Outline each Plasmodium vivax-infected red blood cell.
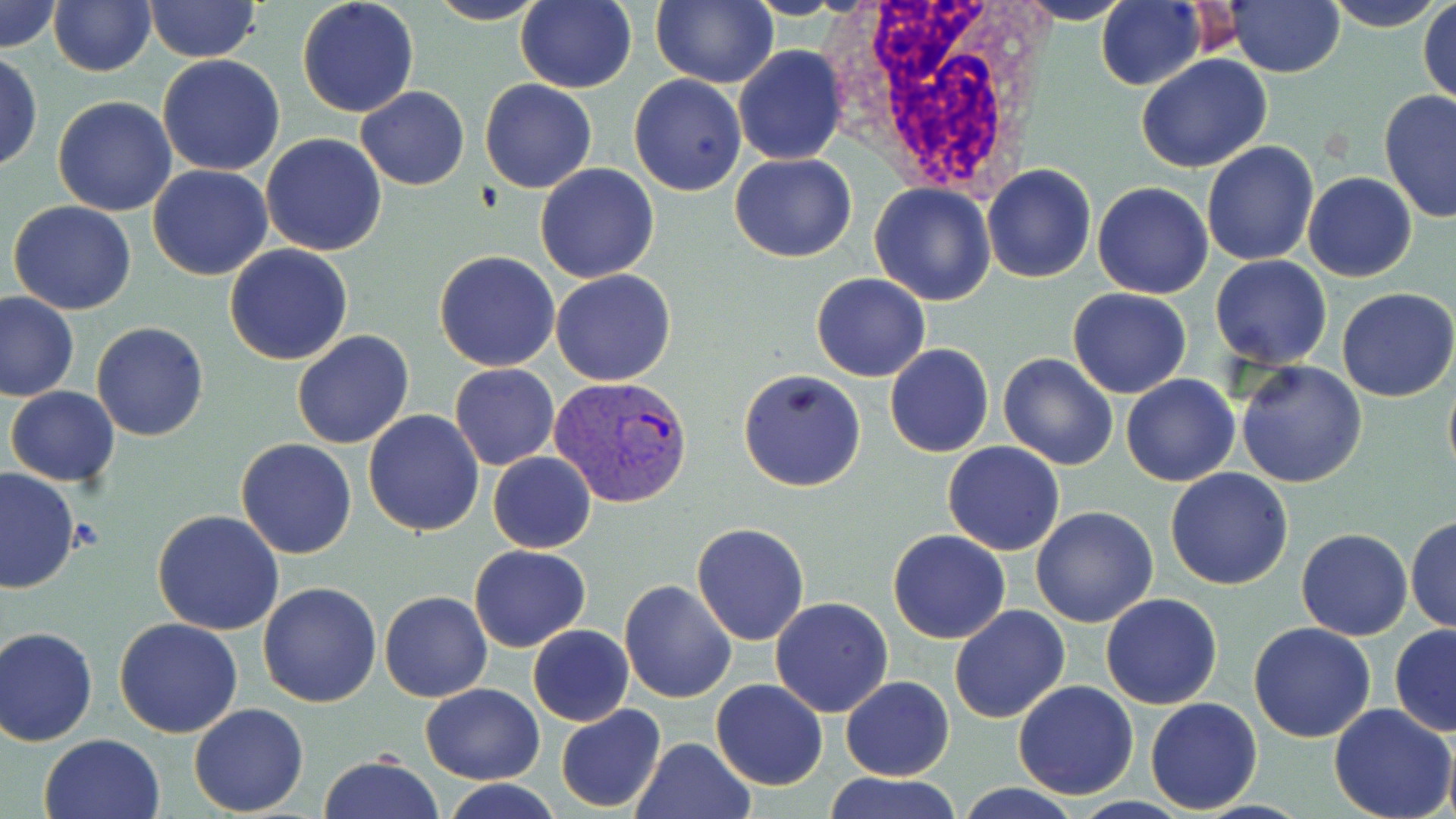

Approximate bounding boxes as [x1, y1, x2, y2] in pixels.
Plasmodium vivax-infected red blood cells: [549, 375, 695, 509].

White blood cell locations: [832, 0, 1054, 196]. Platelet locations: [72, 517, 104, 551]. Uninfected red blood cell locations: [1, 0, 63, 54], [146, 0, 260, 62], [297, 0, 419, 118], [651, 0, 779, 88], [1320, 0, 1445, 31], [48, 1, 156, 76], [424, 1, 550, 26], [515, 1, 636, 93], [1014, 1, 1135, 24], [1096, 1, 1203, 89], [1225, 1, 1344, 77], [1418, 1, 1455, 111], [734, 46, 849, 165], [1, 48, 42, 175], [156, 54, 286, 176], [1136, 54, 1274, 173], [629, 73, 746, 195], [479, 78, 597, 194], [355, 86, 469, 189], [1379, 91, 1456, 223], [52, 96, 179, 217], [260, 133, 387, 256], [1201, 141, 1321, 265], [729, 152, 857, 262], [533, 163, 659, 283], [148, 164, 272, 281], [982, 164, 1097, 284], [1302, 171, 1417, 282], [1092, 181, 1215, 299], [868, 183, 997, 306], [7, 201, 137, 316], [223, 244, 354, 366], [434, 250, 562, 371], [1209, 256, 1332, 370], [551, 268, 675, 386], [810, 273, 930, 382], [1067, 287, 1193, 399], [1336, 287, 1455, 401], [1, 292, 78, 402], [91, 321, 209, 440], [292, 330, 415, 449], [883, 343, 994, 458], [998, 351, 1120, 470], [1236, 359, 1368, 487], [450, 363, 560, 469], [1443, 368, 1456, 488], [738, 369, 866, 492], [1121, 374, 1240, 487], [6, 385, 120, 489], [363, 408, 486, 536], [237, 439, 357, 558], [942, 440, 1065, 557], [488, 451, 596, 553], [1, 468, 78, 594], [1165, 468, 1296, 589], [1030, 506, 1159, 628], [152, 510, 285, 635], [1404, 516, 1455, 634], [691, 522, 811, 645], [1296, 527, 1413, 641], [887, 530, 1012, 644], [468, 545, 590, 651], [619, 580, 738, 702], [258, 581, 382, 706], [380, 590, 493, 704], [1100, 593, 1223, 709], [769, 597, 893, 718], [949, 604, 1070, 724], [112, 619, 243, 738], [1248, 622, 1377, 743], [1389, 623, 1456, 737], [1, 624, 100, 747], [527, 625, 634, 726], [840, 676, 954, 781], [711, 679, 828, 790], [1012, 679, 1139, 799], [420, 683, 546, 782], [1145, 696, 1262, 815], [1329, 703, 1455, 819], [189, 704, 309, 816], [555, 705, 668, 814], [1441, 730, 1456, 819], [39, 734, 165, 819], [630, 736, 757, 819], [318, 753, 442, 819], [822, 771, 963, 819], [444, 780, 564, 818]. Slide-level diagnosis: Plasmodium vivax. Thin blood smear. May-Grünwald-Giemsa-stained preparation. One field of a larger specimen. Optical microscopy. Image is 1456×819 pixels. 1000x magnification.